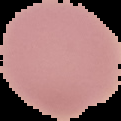
{
  "image_size": "121×121 pixels",
  "result": "negative for Plasmodium parasites",
  "preparation": "thin blood film",
  "image_type": "segmented cell region on a black background"
}